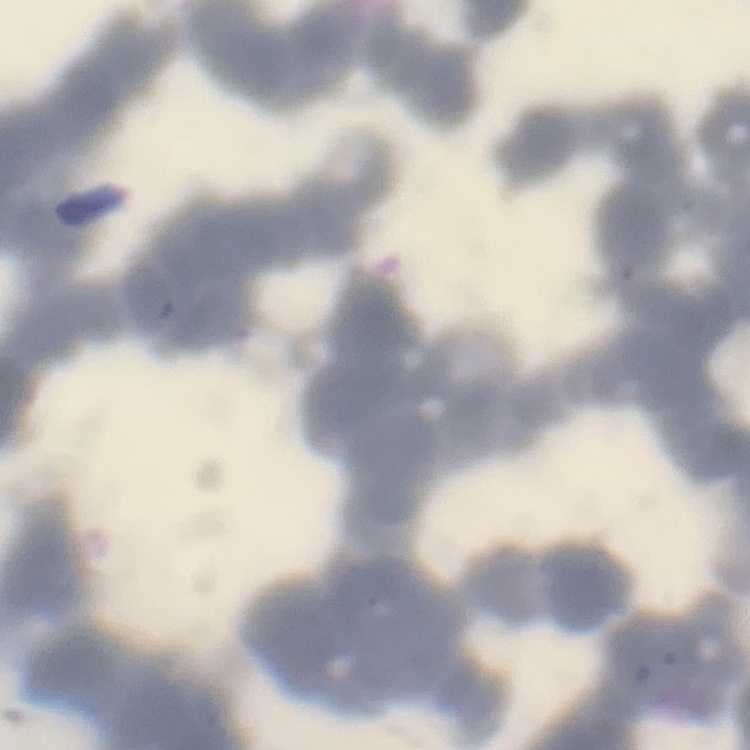

erythrocyte_morphology: rouleaux formation
image_type: square crop of a larger photomicrograph
preparation: thin blood smear
stain: Field's or Giemsa